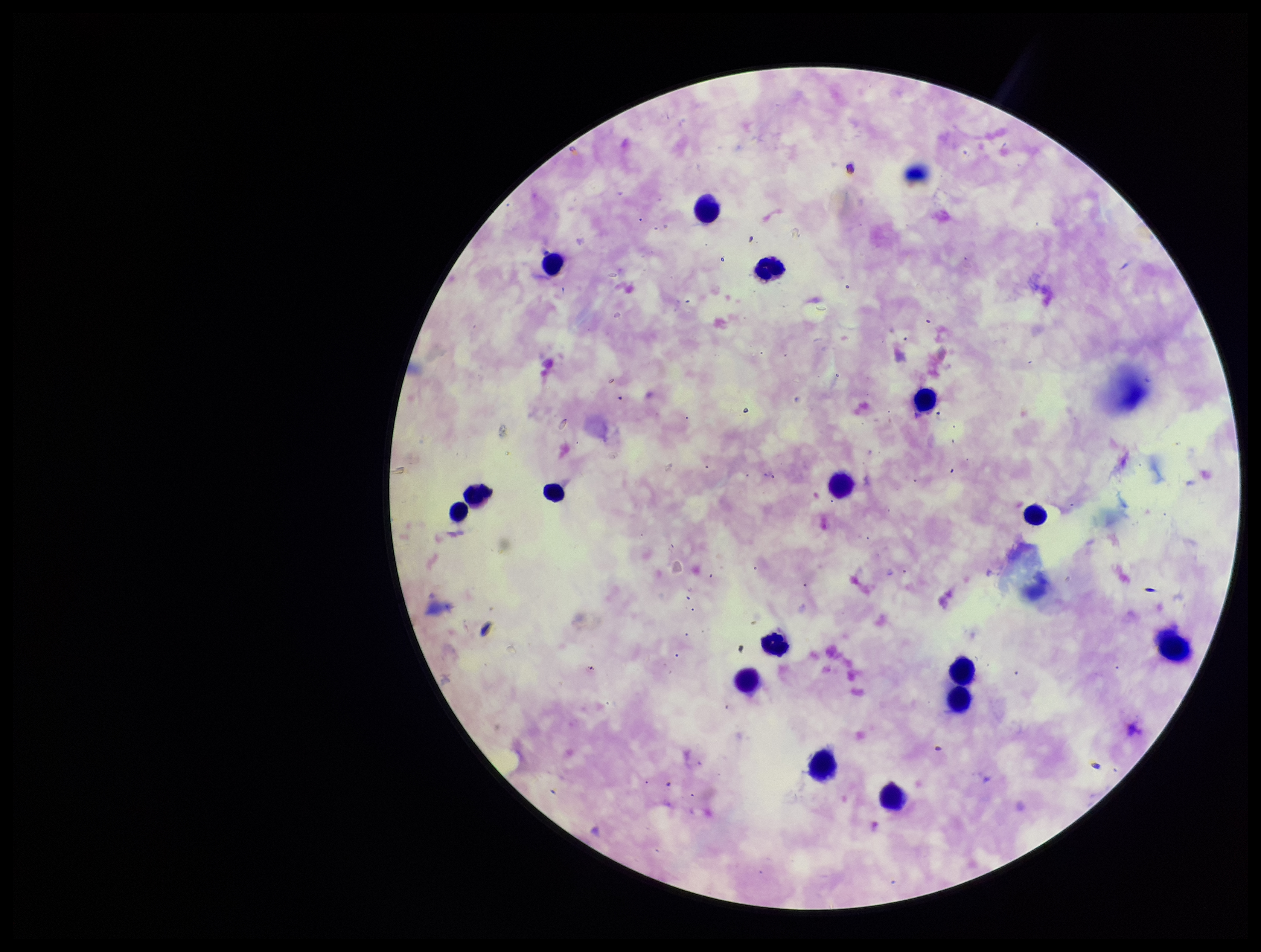
stain: Giemsa
capture: smartphone photograph through the microscope eyepiece
parasite_count: 0
species_reported_for_this_patient: Plasmodium falciparum
patient_malaria_status: infected
plasmodium_parasites: none detected
field_of_view: single
preparation: thick smear
leukocyte_count: 16
image_size: 1261×952 pixels